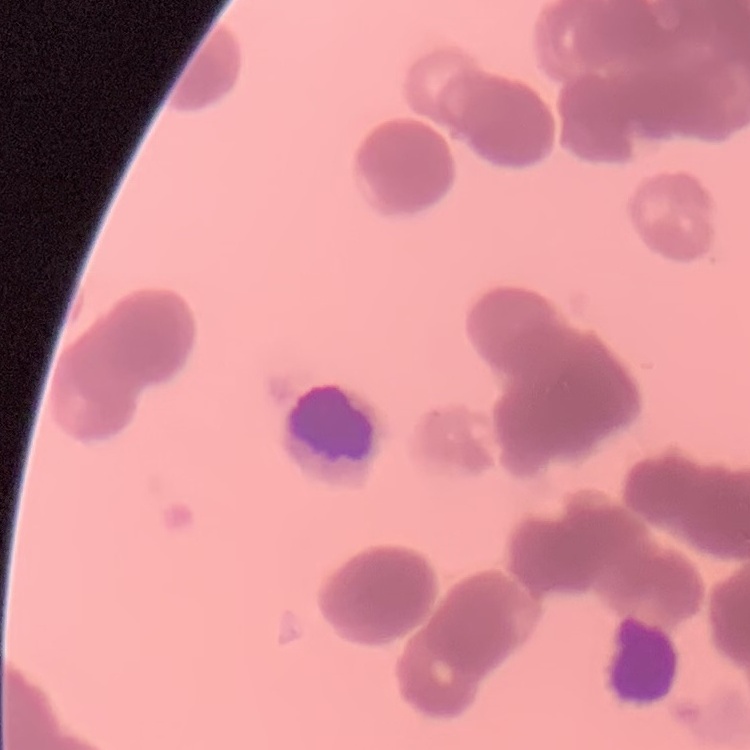

Summary:
  - Red blood cell morphology: rouleaux formation
  - Image type: square crop of a larger photomicrograph
  - Stain: Field's or Giemsa
  - Preparation: thin blood film